Outline each uninfected red blood cell.
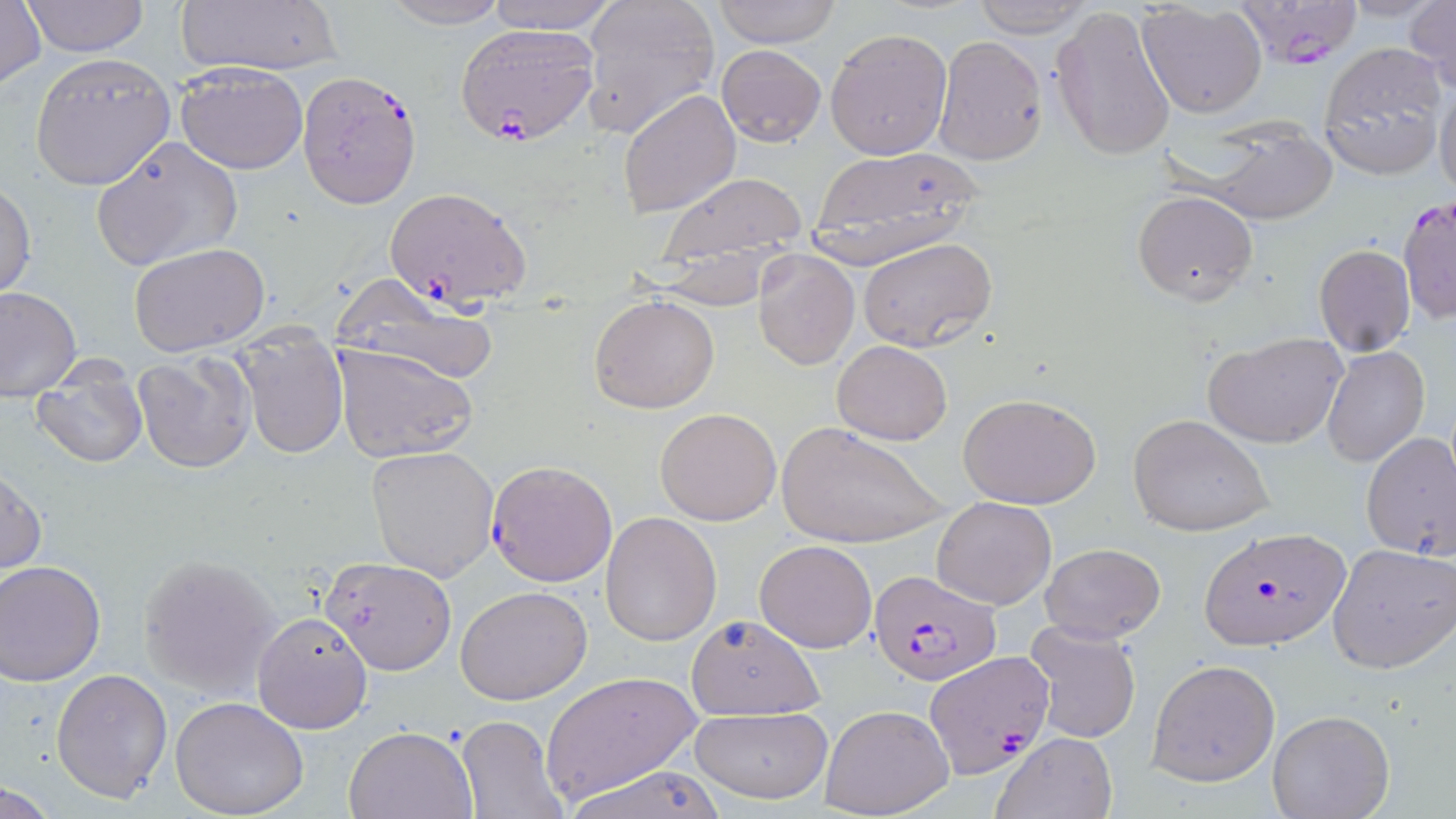

Approximate bounding boxes as (x1, y1, x2, y2) in pixels.
Uninfected red blood cells: (0, 0, 47, 91), (21, 0, 149, 57), (175, 0, 342, 79), (379, 0, 514, 29), (486, 0, 619, 32), (578, 0, 721, 141), (710, 0, 843, 48), (970, 0, 1093, 38), (1406, 0, 1456, 93), (1135, 2, 1268, 119), (1051, 5, 1178, 162), (825, 26, 952, 160), (933, 35, 1049, 166), (1320, 41, 1448, 180), (716, 43, 827, 148), (28, 51, 177, 190), (174, 63, 309, 174), (1435, 79, 1456, 200), (617, 88, 742, 218), (90, 135, 243, 272), (1203, 135, 1340, 224), (807, 149, 983, 265), (657, 172, 809, 260), (0, 180, 36, 301), (1132, 188, 1259, 305), (858, 237, 998, 352), (129, 242, 270, 354), (1314, 244, 1416, 356), (753, 251, 859, 369), (0, 285, 80, 396), (335, 289, 506, 386), (589, 294, 719, 413), (1203, 331, 1348, 450), (832, 339, 952, 446), (236, 341, 348, 459), (331, 342, 480, 463), (1322, 346, 1430, 466), (130, 354, 256, 474), (32, 381, 148, 469), (956, 391, 1104, 511), (655, 407, 783, 526), (1128, 414, 1275, 538), (777, 420, 949, 550), (1361, 432, 1456, 561), (366, 445, 500, 582), (1, 467, 47, 580), (931, 496, 1056, 608), (602, 511, 722, 647), (754, 538, 878, 653), (1328, 543, 1456, 673), (1041, 544, 1165, 642), (139, 554, 281, 699), (320, 556, 456, 675), (1, 562, 106, 686), (455, 584, 593, 705), (252, 610, 373, 734), (684, 614, 826, 720), (1023, 619, 1143, 745), (1147, 659, 1280, 787), (50, 668, 173, 804), (540, 673, 703, 803), (170, 695, 310, 818), (820, 704, 953, 817), (689, 705, 833, 805), (1267, 710, 1396, 819), (457, 716, 568, 819), (343, 724, 478, 818), (992, 732, 1117, 819), (561, 764, 727, 819), (1, 782, 62, 816).

slide_level_diagnosis: Plasmodium falciparum
preparation: thin blood film
stain: May-Grünwald-Giemsa
modality: optical microscopy
field_of_view: one of a larger specimen
image_size: 1456×819 pixels
plasmodium_falciparum_infected_red_blood_cell_locations: 'approximate bounding boxes as (x1, y1, x2, y2) in pixels: (1230, 0, 1362, 68), (454, 23, 600, 145), (296, 70, 422, 209), (384, 186, 533, 306), (1396, 194, 1456, 325), (485, 457, 618, 587), (1199, 525, 1351, 653), (868, 567, 1001, 683), (924, 650, 1054, 779)'
magnification: 1000x